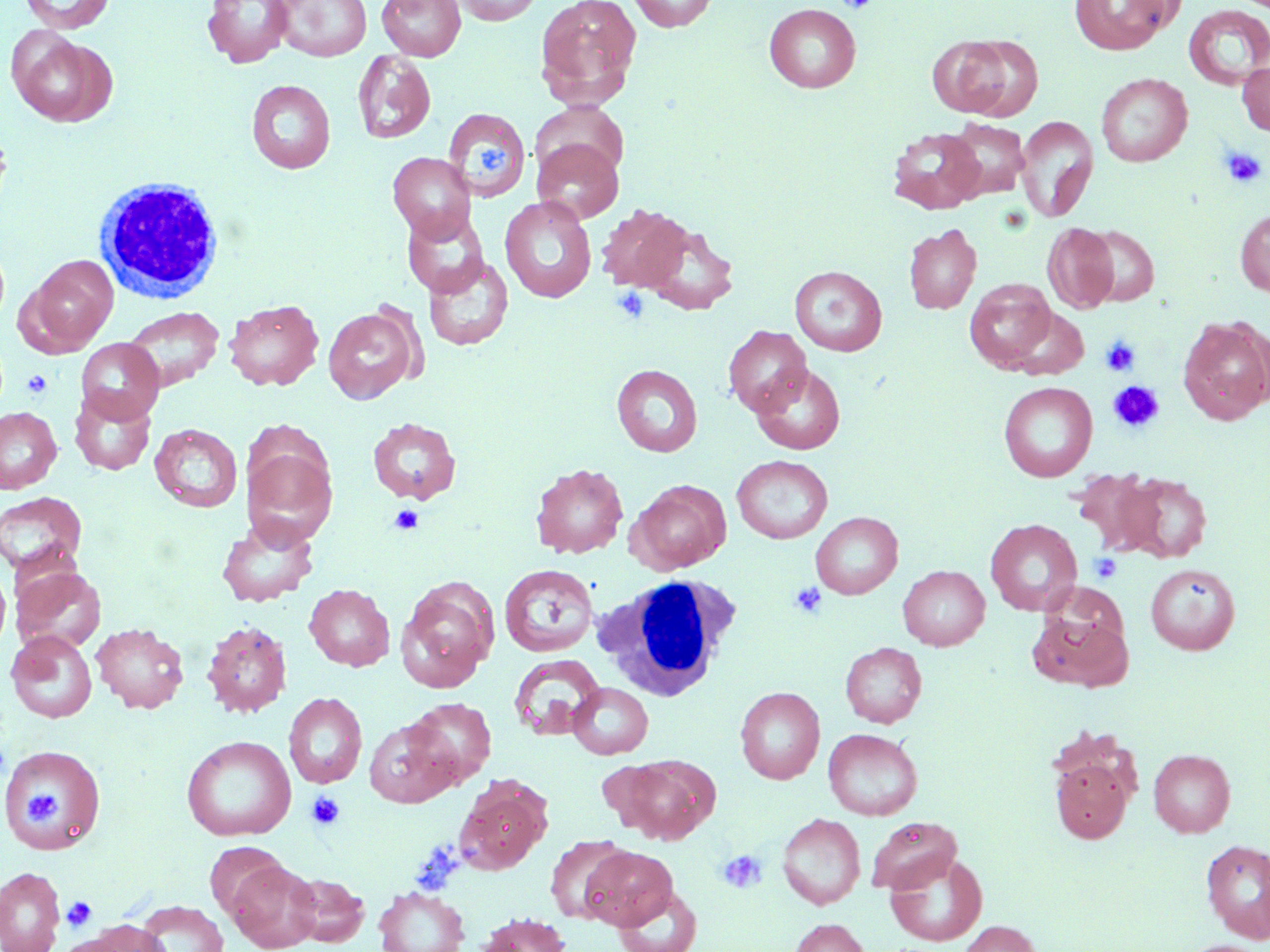

{
  "slide_level_diagnosis": "negative for blood parasites",
  "field_of_view": "one of a larger specimen",
  "modality": "optical microscopy",
  "preparation": "thin blood smear",
  "white_blood_cell_locations": "approximate bounding boxes as (x1, y1, x2, y2) in pixels: (95, 176, 226, 305), (593, 575, 739, 702)",
  "uninfected_red_blood_cell_locations": "approximate bounding boxes as (x1, y1, x2, y2) in pixels: (20, 0, 115, 32), (202, 0, 293, 68), (272, 0, 371, 61), (377, 0, 466, 61), (452, 0, 544, 25), (627, 0, 718, 32), (1068, 0, 1178, 54), (535, 1, 643, 109), (764, 3, 861, 92), (1184, 5, 1270, 90), (10, 33, 117, 127), (927, 36, 1025, 120), (352, 51, 437, 145), (1237, 60, 1270, 137), (1096, 72, 1192, 167), (246, 80, 336, 174), (531, 102, 630, 187), (443, 107, 530, 202), (1016, 116, 1098, 223), (947, 118, 1030, 200), (0, 120, 13, 216), (888, 128, 986, 215), (532, 137, 624, 224), (388, 152, 476, 241), (500, 196, 597, 303), (597, 204, 694, 293), (1235, 208, 1270, 297), (401, 209, 488, 297), (639, 223, 739, 315), (1042, 223, 1119, 313), (904, 224, 982, 314), (1081, 225, 1159, 306), (422, 254, 514, 351), (22, 255, 118, 354), (790, 266, 887, 356), (964, 279, 1056, 371), (224, 299, 324, 390), (123, 306, 225, 391), (323, 306, 419, 403), (1004, 307, 1089, 379), (1178, 316, 1270, 424), (723, 325, 812, 416), (76, 338, 165, 423), (611, 364, 702, 456), (751, 364, 845, 454), (998, 381, 1098, 482), (69, 388, 156, 475), (0, 407, 62, 494), (367, 416, 461, 505), (149, 423, 243, 513), (242, 442, 337, 546), (731, 454, 833, 543), (530, 463, 629, 558), (1071, 468, 1168, 559), (1114, 472, 1212, 562), (628, 480, 730, 573), (0, 491, 87, 575), (810, 512, 903, 599), (216, 517, 318, 606), (985, 518, 1083, 616), (0, 562, 11, 653), (1145, 563, 1240, 654), (11, 564, 106, 655), (499, 564, 598, 657), (898, 565, 989, 650), (395, 582, 496, 692), (305, 584, 395, 671), (1027, 601, 1133, 692), (202, 621, 292, 718), (91, 623, 189, 713), (6, 630, 97, 724), (840, 642, 927, 728), (509, 654, 604, 739), (568, 683, 653, 758), (735, 686, 825, 784), (284, 692, 367, 789), (406, 697, 496, 786), (364, 717, 461, 808), (823, 728, 923, 820), (181, 735, 296, 841), (2, 744, 105, 851), (1148, 749, 1235, 836), (614, 754, 720, 843), (1050, 755, 1133, 843), (454, 778, 551, 875), (777, 813, 866, 909), (866, 817, 962, 894), (545, 834, 632, 923), (1201, 839, 1270, 943), (205, 841, 291, 922), (581, 846, 678, 930), (885, 851, 988, 947), (227, 858, 322, 951), (0, 865, 66, 952), (286, 873, 369, 947), (614, 885, 702, 952), (374, 886, 470, 952), (134, 900, 229, 951), (475, 912, 573, 952), (790, 918, 870, 952), (74, 919, 168, 952), (958, 920, 1042, 952), (1176, 939, 1268, 952)",
  "stain": "May-Grünwald-Giemsa",
  "platelet_locations": "approximate bounding boxes as (x1, y1, x2, y2) in pixels: (835, 0, 881, 14), (1220, 146, 1266, 187), (611, 285, 650, 324), (1100, 337, 1140, 377), (22, 370, 53, 398), (1108, 380, 1164, 434), (388, 505, 424, 535), (1090, 553, 1123, 584), (789, 581, 828, 619), (27, 788, 57, 825), (307, 791, 345, 830), (717, 850, 767, 894), (61, 896, 97, 933)",
  "magnification": "1000x",
  "image_size": "1270×952 pixels"
}